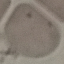
{
  "malaria_status": "uninfected",
  "capture": "smartphone camera at the microscope eyepiece",
  "preparation": "thin smear",
  "image_type": "cell patch, automatically extracted from a larger field of view and resized to 64 × 64 pixels",
  "stain": "Giemsa"
}